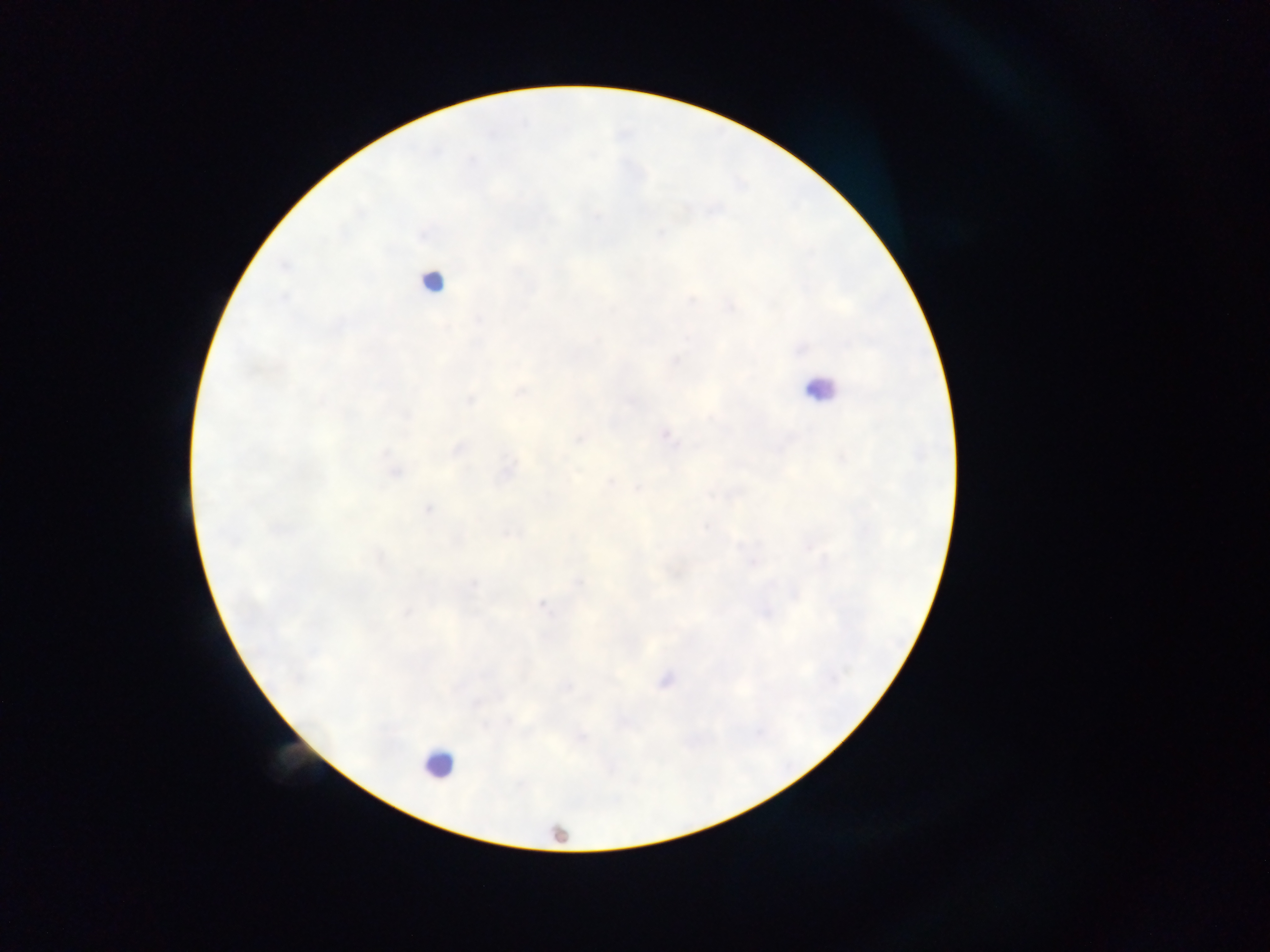

Approximate centers as x y in pixels.
Summary:
  - Leukocyte locations: 433 283; 819 389; 438 764; 557 836
  - Plasmodium parasite locations: 518 391; 665 434; 578 439; 456 449; 506 469; 394 470; 639 487; 428 509; 542 604; 664 680
  - Capture: mobile-phone photograph through a microscope
  - Field of view: single
  - Country: Ghana
  - Preparation: thick blood smear
  - Image size: 1270×952 pixels